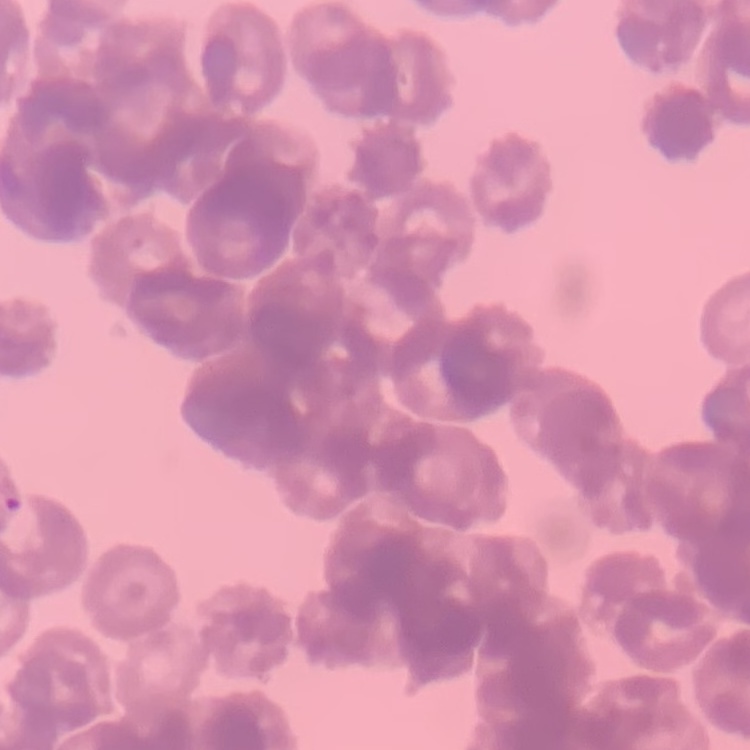
{
  "erythrocyte_morphology": "rouleaux formation",
  "image_type": "one tile cut from a larger photomicrograph",
  "stain": "Field's or Giemsa",
  "preparation": "thin blood smear"
}